Locate every blood parasite and identify its species.
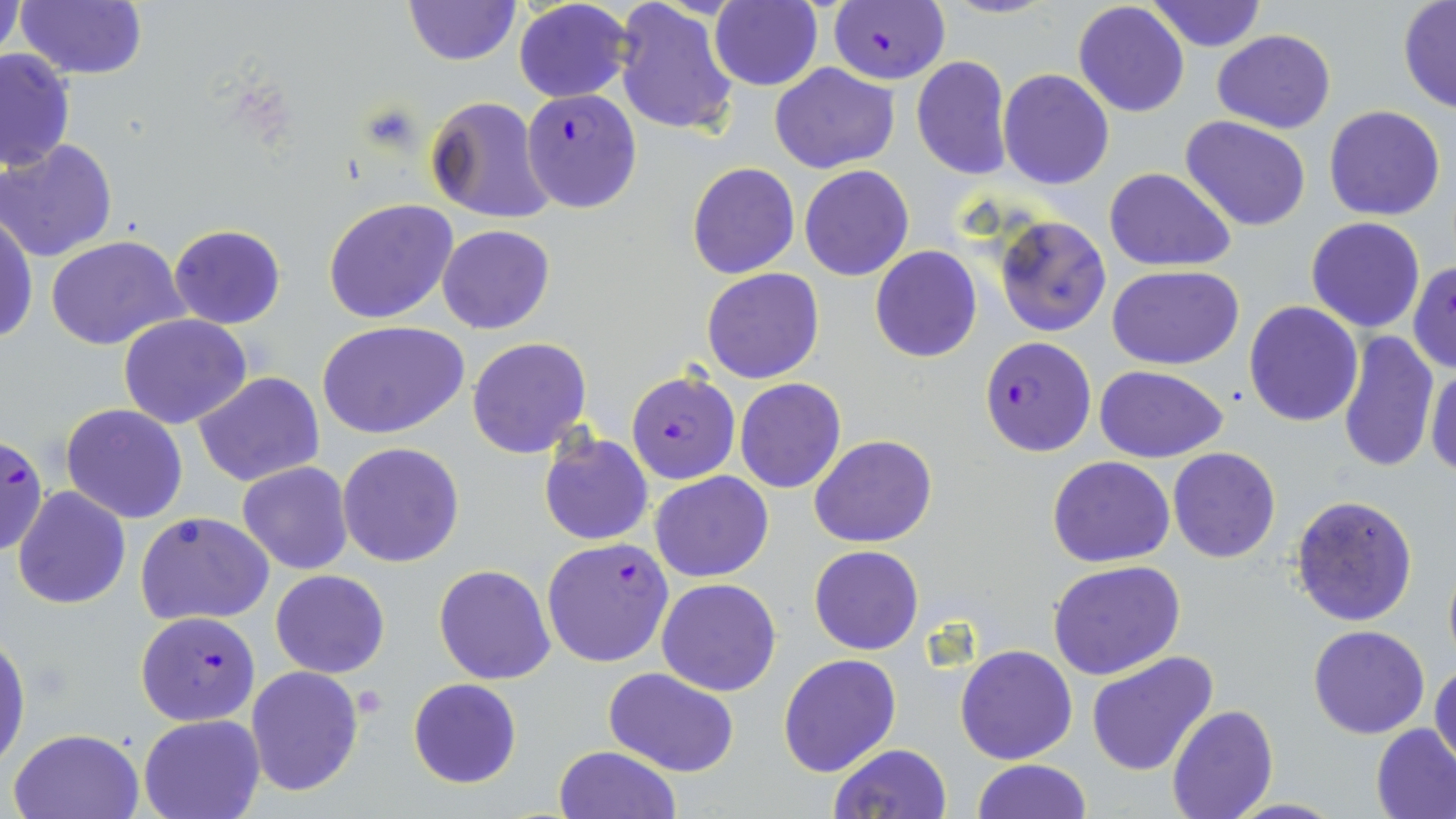
Approximate bounding boxes as (x1,y1)-(x2,y2) corner pairs in pixels.
Plasmodium falciparum-infected red blood cells: (828,0)-(948,84), (521,89)-(643,212), (979,337)-(1096,457), (627,370)-(741,485), (1,433)-(44,558), (541,538)-(674,668), (135,611)-(260,727).
No Plasmodium ovale, Plasmodium malariae, Plasmodium vivax, Babesia divergens, or Trypanosoma brucei observed.

Summary:
  - Platelet locations: (356,685)-(386,718)
  - Uninfected red blood cell locations: (15,0)-(150,81), (402,0)-(519,67), (511,0)-(635,104), (613,0)-(741,138), (1148,0)-(1266,52), (0,1)-(24,65), (707,1)-(822,92), (1073,1)-(1190,118), (1398,1)-(1456,114), (1212,30)-(1336,132), (0,46)-(75,175), (911,55)-(1012,179), (769,61)-(900,174), (998,68)-(1113,190), (425,95)-(558,224), (1323,105)-(1446,221), (1180,116)-(1312,233), (0,139)-(119,263), (687,163)-(799,279), (799,165)-(914,281), (1103,166)-(1237,272), (323,198)-(458,323), (1,213)-(37,345), (994,215)-(1112,338), (1305,217)-(1427,333), (167,224)-(287,329), (437,224)-(555,334), (46,236)-(189,352), (870,245)-(982,363), (1409,260)-(1456,374), (1107,265)-(1245,368), (701,268)-(824,384), (1244,300)-(1363,426), (117,313)-(252,430), (319,320)-(470,440), (1338,328)-(1439,474), (467,337)-(594,459), (1426,363)-(1455,477), (1094,364)-(1229,462), (194,372)-(325,488), (734,378)-(846,494), (61,403)-(188,523), (537,431)-(653,546), (810,435)-(937,548), (338,442)-(465,568), (1168,447)-(1281,563), (1048,456)-(1175,568), (237,461)-(354,574), (650,471)-(773,582), (12,485)-(130,609), (1290,494)-(1419,627), (136,510)-(273,626), (809,544)-(924,655), (1442,549)-(1456,670), (1048,559)-(1187,679), (433,564)-(556,684), (270,568)-(391,678), (657,578)-(782,696), (1308,624)-(1431,740), (0,627)-(30,769), (954,643)-(1078,765), (1086,651)-(1217,776), (777,653)-(901,777), (1429,658)-(1456,768), (245,665)-(365,797), (604,668)-(739,776), (408,678)-(521,788), (1167,704)-(1279,819), (139,715)-(263,819), (1371,723)-(1456,819), (9,727)-(145,819), (827,743)-(951,819), (553,746)-(681,819), (971,758)-(1091,818)
  - Slide-level diagnosis: Plasmodium falciparum
  - Field of view: single
  - Preparation: thin blood smear
  - Modality: light microscopy
  - Magnification: 1000x
  - Stain: May-Grünwald-Giemsa
  - Image size: 1456×819 pixels